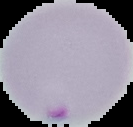 Result: malaria parasites identified. Image is 133×127 pixels. Cell region segmented out of the field of view; the surrounding area is masked to black. From a thin blood smear.